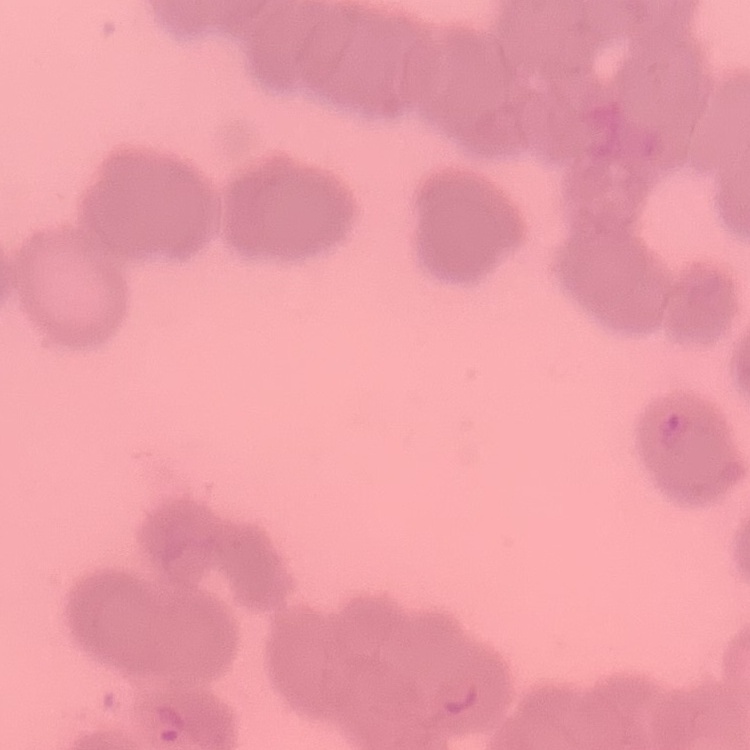 The erythrocytes exhibit rouleaux formation. Thin peripheral smear. Square crop of a larger photomicrograph. Stained with either Field's or Giemsa.